Name the parasite shown.
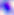
This is Toxoplasma gondii.

Summary:
  - Magnification: 400x
  - Modality: micrograph